Assess the morphology of the red blood cells.
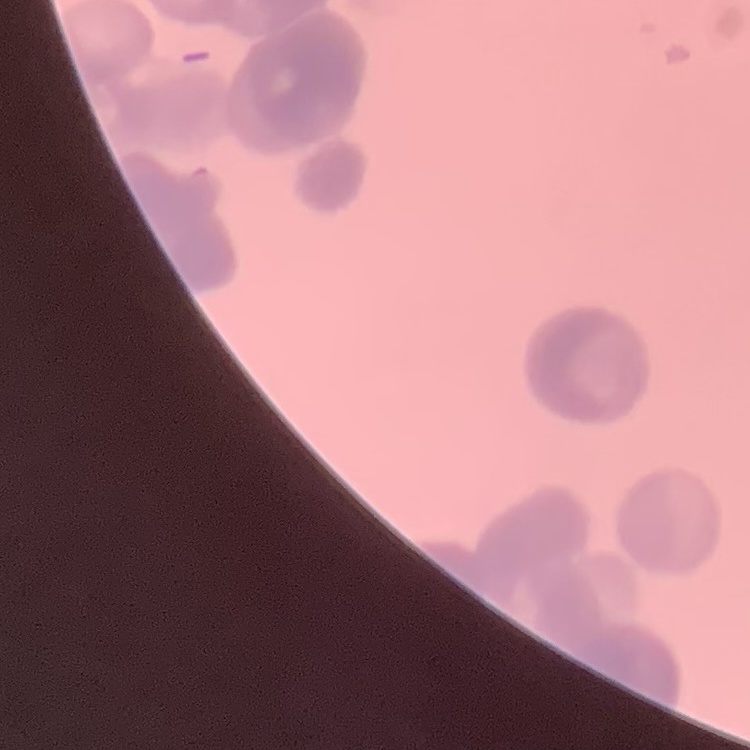

They show rouleaux formation.

Summary:
  - Stain: Field's or Giemsa
  - Image type: one tile cut from a larger photomicrograph
  - Preparation: thin peripheral smear